Assess this cell for malaria.
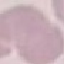
Uninfected.

stain = Giemsa
image type = automatically extracted cell patch, resized to 64 × 64 pixels
capture = smartphone camera at the microscope eyepiece
preparation = thin blood smear